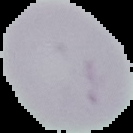
Summary:
  - Image size: 133×133 pixels
  - Image type: segmented cell region on a black background
  - Preparation: thin blood smear
  - Malaria status: uninfected